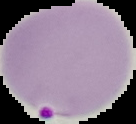
From a thin blood smear. Result: malaria parasites identified. Image is 136×124 pixels. Segmented cell region on a black background.